Give the extent of all Babesia divergens-infected red blood cells.
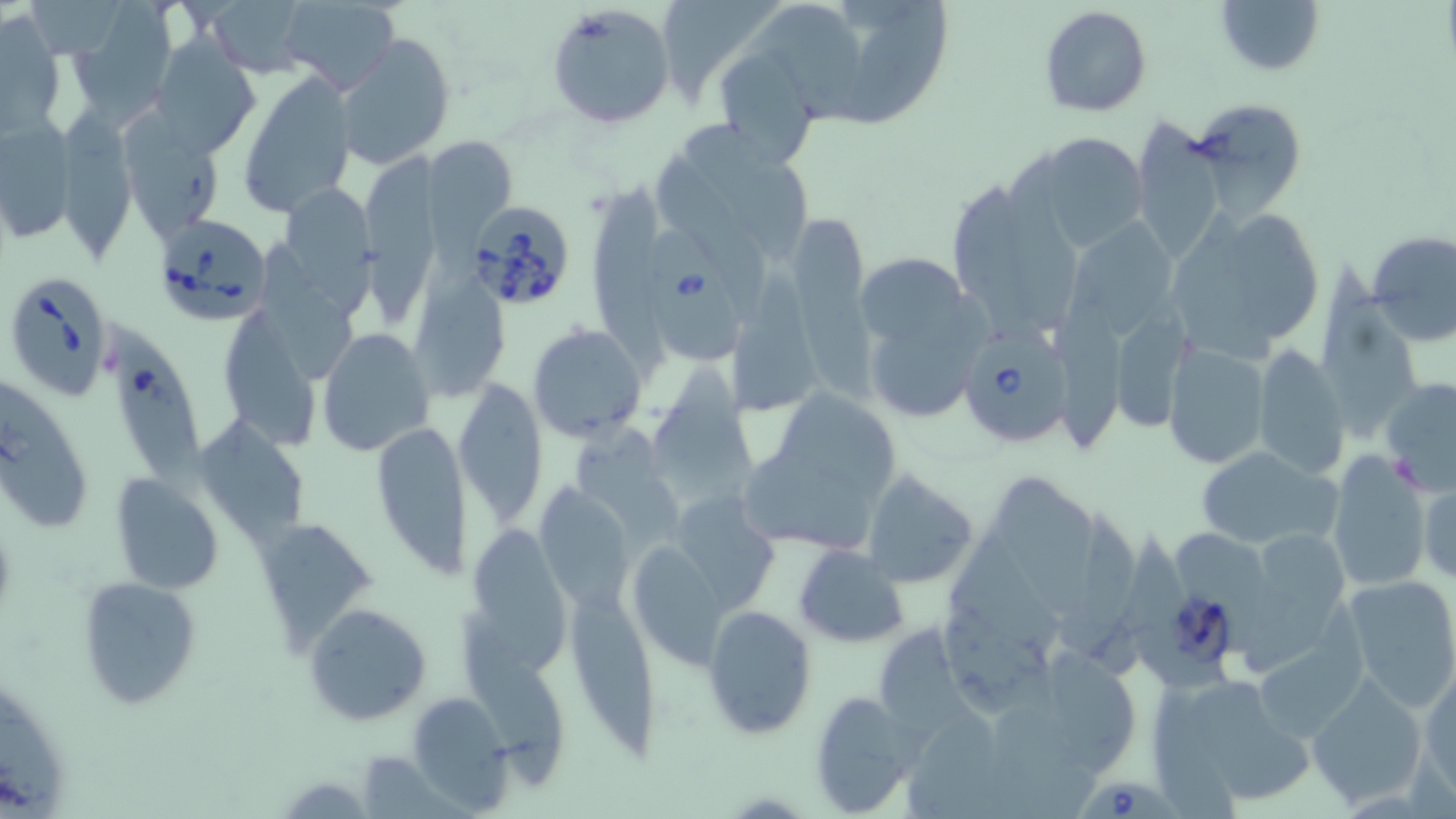

Approximate bounding boxes as named x1/y1/x2/y2 corners in pixels.
Babesia divergens-infected red blood cells: (x1=467, y1=201, x2=578, y2=312), (x1=152, y1=214, x2=272, y2=328), (x1=648, y1=230, x2=746, y2=363), (x1=5, y1=271, x2=117, y2=402), (x1=109, y1=322, x2=216, y2=501), (x1=957, y1=325, x2=1076, y2=449), (x1=1081, y1=774, x2=1186, y2=819).

slide-level diagnosis = Babesia divergens
field of view = single
magnification = 1000x
stain = May-Grünwald-Giemsa
uninfected red blood cell locations = approximate bounding boxes as named x1/y1/x2/y2 corners in pixels: (x1=279, y1=0, x2=400, y2=94), (x1=1212, y1=0, x2=1324, y2=77), (x1=202, y1=1, x2=315, y2=76), (x1=664, y1=3, x2=777, y2=115), (x1=751, y1=3, x2=878, y2=127), (x1=66, y1=4, x2=178, y2=127), (x1=544, y1=4, x2=675, y2=131), (x1=842, y1=5, x2=952, y2=127), (x1=1038, y1=5, x2=1152, y2=117), (x1=2, y1=12, x2=65, y2=133), (x1=334, y1=32, x2=455, y2=171), (x1=149, y1=34, x2=261, y2=161), (x1=720, y1=52, x2=814, y2=167), (x1=237, y1=70, x2=357, y2=218), (x1=1189, y1=96, x2=1308, y2=220), (x1=56, y1=112, x2=139, y2=262), (x1=1, y1=116, x2=79, y2=240), (x1=1130, y1=121, x2=1229, y2=268), (x1=685, y1=123, x2=810, y2=263), (x1=435, y1=132, x2=527, y2=279), (x1=1018, y1=134, x2=1153, y2=254), (x1=365, y1=150, x2=455, y2=333), (x1=664, y1=159, x2=777, y2=310), (x1=282, y1=176, x2=390, y2=320), (x1=590, y1=182, x2=672, y2=391), (x1=1166, y1=202, x2=1327, y2=359), (x1=789, y1=218, x2=883, y2=407), (x1=1075, y1=221, x2=1181, y2=342), (x1=1366, y1=229, x2=1456, y2=346), (x1=263, y1=244, x2=356, y2=382), (x1=856, y1=257, x2=977, y2=349), (x1=1309, y1=264, x2=1429, y2=444), (x1=723, y1=269, x2=833, y2=418), (x1=411, y1=272, x2=512, y2=398), (x1=1112, y1=300, x2=1204, y2=433), (x1=1053, y1=302, x2=1135, y2=456), (x1=226, y1=313, x2=321, y2=452), (x1=527, y1=323, x2=647, y2=443), (x1=317, y1=327, x2=434, y2=459), (x1=1162, y1=345, x2=1269, y2=469), (x1=1252, y1=345, x2=1349, y2=479), (x1=652, y1=368, x2=756, y2=505), (x1=1381, y1=376, x2=1456, y2=495), (x1=0, y1=380, x2=92, y2=534), (x1=452, y1=385, x2=548, y2=526), (x1=775, y1=388, x2=909, y2=493), (x1=193, y1=413, x2=309, y2=551), (x1=369, y1=419, x2=476, y2=582), (x1=575, y1=428, x2=685, y2=551), (x1=1192, y1=445, x2=1342, y2=553), (x1=1324, y1=450, x2=1434, y2=593), (x1=862, y1=470, x2=980, y2=590), (x1=110, y1=473, x2=225, y2=596), (x1=991, y1=474, x2=1102, y2=619), (x1=1417, y1=475, x2=1456, y2=586), (x1=535, y1=484, x2=636, y2=613), (x1=1053, y1=507, x2=1157, y2=678), (x1=256, y1=516, x2=380, y2=655), (x1=466, y1=516, x2=575, y2=674), (x1=1243, y1=533, x2=1347, y2=676), (x1=625, y1=537, x2=736, y2=668), (x1=794, y1=543, x2=909, y2=648), (x1=76, y1=575, x2=198, y2=709), (x1=1340, y1=575, x2=1456, y2=709), (x1=570, y1=582, x2=668, y2=761), (x1=303, y1=603, x2=432, y2=728), (x1=702, y1=604, x2=818, y2=739), (x1=946, y1=606, x2=1067, y2=721), (x1=454, y1=619, x2=573, y2=790), (x1=876, y1=627, x2=987, y2=747), (x1=1420, y1=668, x2=1455, y2=798), (x1=1306, y1=674, x2=1428, y2=809), (x1=0, y1=681, x2=66, y2=819), (x1=1191, y1=685, x2=1324, y2=806), (x1=806, y1=690, x2=917, y2=815), (x1=408, y1=691, x2=510, y2=807)
modality = light microscopy
preparation = thin blood film
image size = 1456×819 pixels